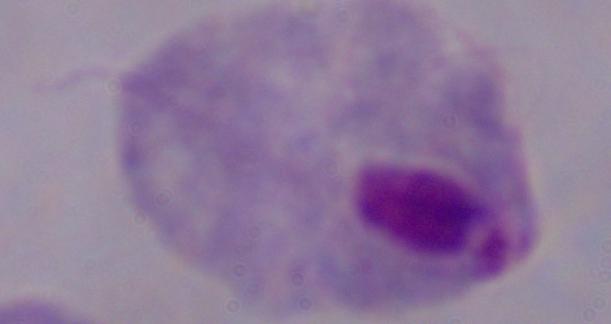

magnification: 1000x
identification: trichomonad
modality: micrograph